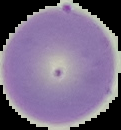

Summary:
  - Result: no Plasmodium parasites detected
  - Preparation: thin blood film
  - Image type: segmented cell region on a black background
  - Image size: 121×130 pixels